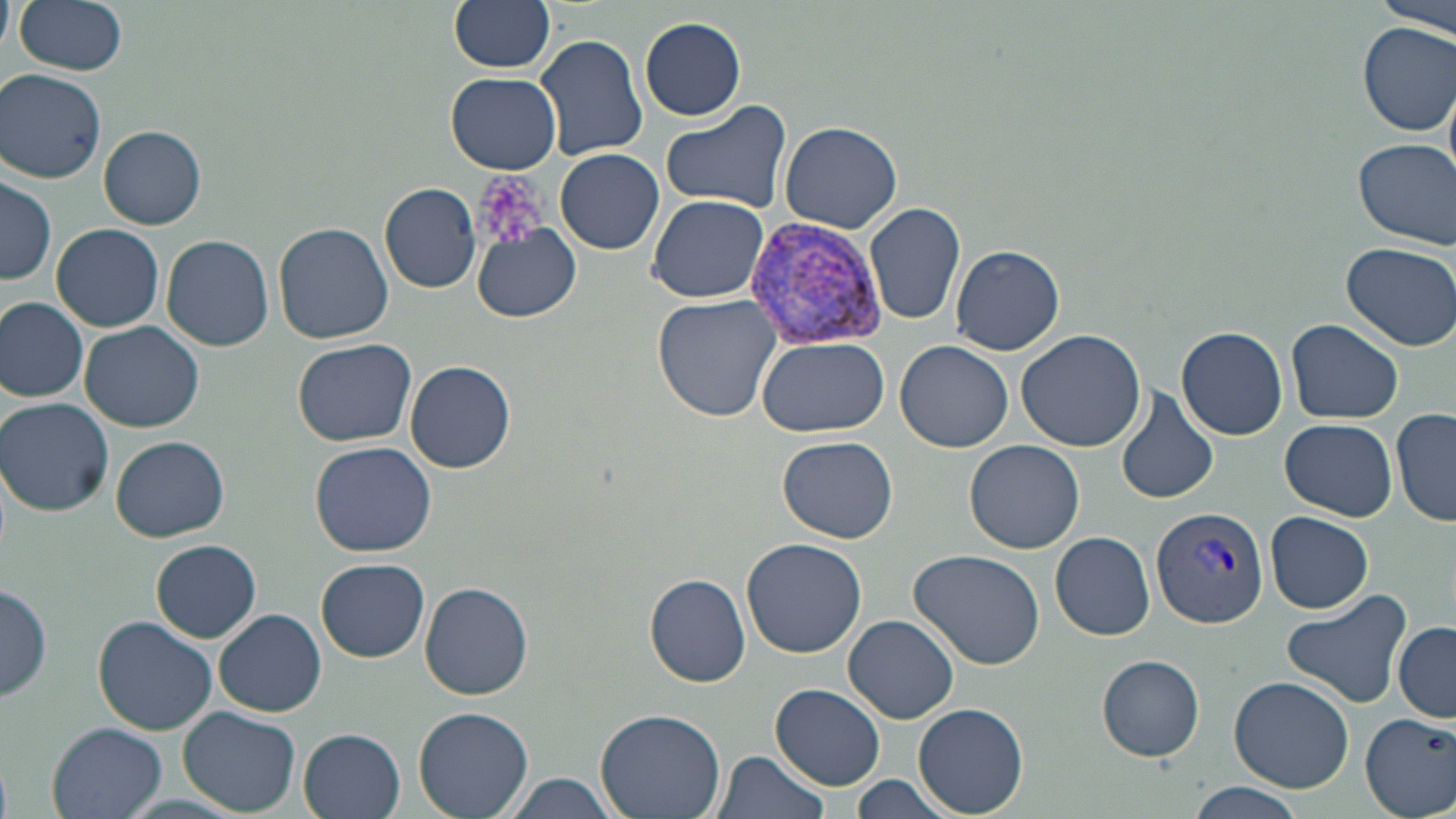
Summary:
  - Coordinate format: approximate bounding boxes as (x1,y1)-(x2,y2) corner pairs in pixels
  - Plasmodium vivax-infected red blood cell locations: (747,217)-(886,347), (1151,506)-(1269,627)
  - Uninfected red blood cell locations: (0,0)-(15,54), (16,0)-(127,76), (449,0)-(556,73), (1377,0)-(1456,37), (640,17)-(746,122), (1358,22)-(1456,136), (534,33)-(651,161), (1,69)-(108,184), (447,73)-(562,173), (660,102)-(793,212), (781,121)-(902,234), (98,125)-(206,229), (1354,138)-(1455,249), (556,147)-(664,254), (1,177)-(56,286), (380,182)-(481,293), (334,193)-(443,309), (646,194)-(770,304), (863,202)-(968,328), (275,222)-(393,345), (52,223)-(165,331), (471,225)-(581,322), (161,234)-(274,351), (1340,242)-(1456,350), (950,245)-(1064,356), (652,295)-(783,425), (0,296)-(89,403), (1285,319)-(1405,424), (80,321)-(204,432), (1177,326)-(1288,440), (1016,328)-(1144,452), (758,336)-(888,437), (292,338)-(419,447), (895,340)-(1016,453), (1142,343)-(1253,476), (406,360)-(514,472), (1114,387)-(1219,507), (1,398)-(116,516), (1391,408)-(1455,528), (1281,417)-(1396,523), (112,435)-(230,542), (777,436)-(899,543), (965,439)-(1086,553), (310,440)-(438,556), (1264,511)-(1374,614), (1049,531)-(1156,641), (741,538)-(867,658), (151,540)-(261,643), (908,548)-(1046,670), (318,558)-(430,661), (645,573)-(751,688), (0,580)-(53,703), (419,581)-(534,699), (1282,587)-(1412,710), (214,609)-(326,717), (92,614)-(219,736), (844,614)-(959,724), (1393,622)-(1455,723), (1098,655)-(1205,760), (1228,676)-(1354,792), (771,684)-(884,790), (914,703)-(1029,816), (179,706)-(301,814), (414,707)-(532,819), (595,707)-(724,819), (1361,711)-(1456,817), (47,721)-(168,819), (299,728)-(406,818), (712,749)-(832,819), (504,774)-(620,818), (849,776)-(954,819), (1185,783)-(1305,819)
  - Platelet locations: (472,171)-(550,252)
  - Slide-level diagnosis: Plasmodium vivax
  - Stain: May-Grünwald-Giemsa
  - Magnification: 1000x
  - Preparation: thin blood smear
  - Image size: 1456×819 pixels
  - Field of view: one of a larger specimen
  - Modality: light microscopy